Locate every blood parasite and identify its species.
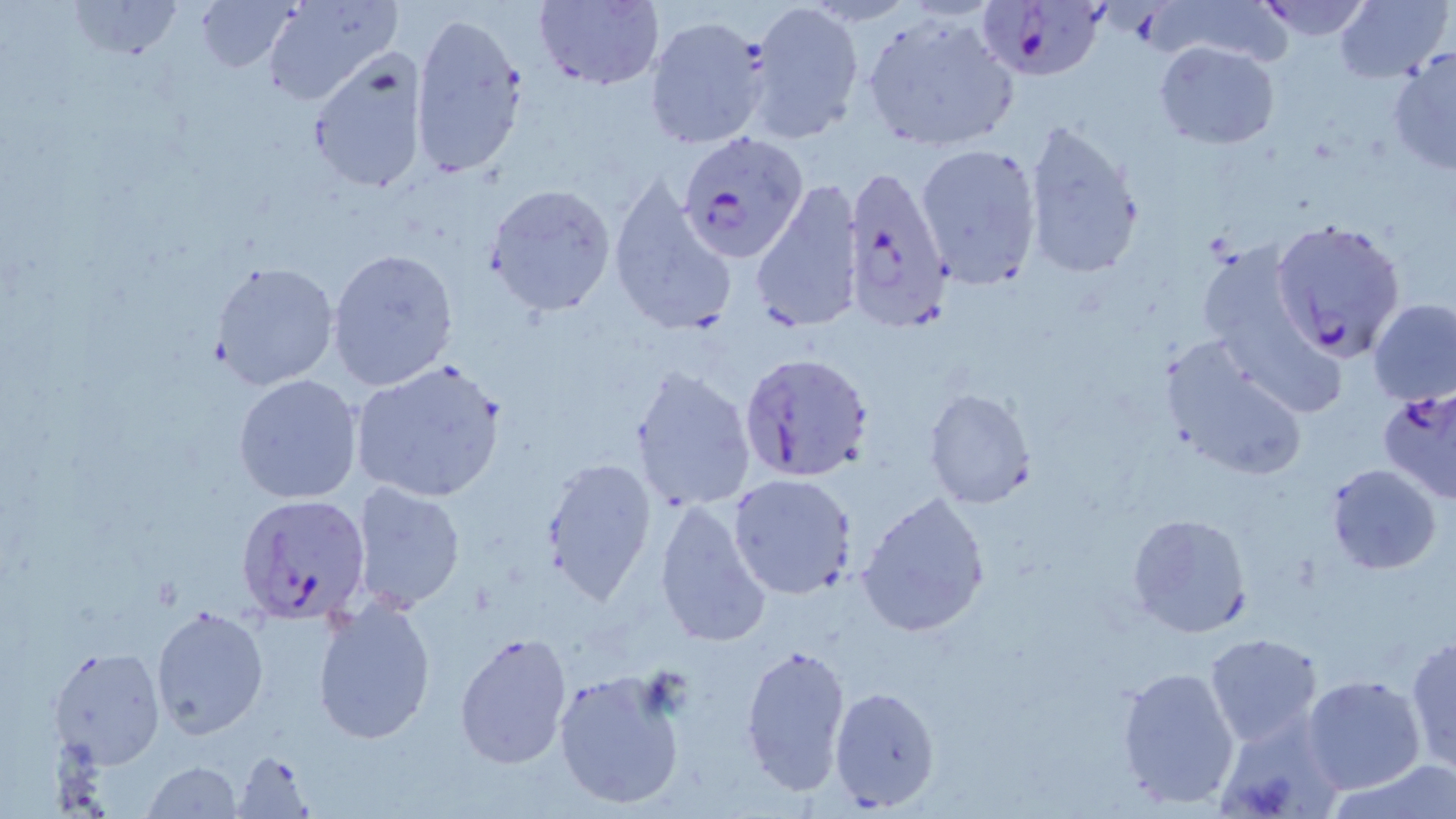

Approximate bounding boxes as (x1,y1)-(x2,y2) corner pairs in pixels.
Plasmodium falciparum-infected red blood cells: (980,1)-(1110,83), (680,132)-(808,262), (839,162)-(956,334), (1270,218)-(1408,361), (739,351)-(877,484), (1374,384)-(1456,509), (236,493)-(372,625).
No Plasmodium ovale, Plasmodium malariae, Plasmodium vivax, Babesia divergens, or Trypanosoma brucei observed.

Summary:
  - Uninfected red blood cell locations: (66,0)-(185,60), (194,0)-(299,74), (260,0)-(400,107), (532,0)-(664,90), (1254,0)-(1377,41), (1336,1)-(1450,82), (745,2)-(866,142), (407,11)-(530,179), (862,13)-(1018,152), (645,15)-(771,150), (1154,40)-(1281,150), (1387,45)-(1456,177), (305,52)-(431,194), (1020,118)-(1145,283), (915,142)-(1042,287), (608,177)-(736,336), (750,180)-(863,334), (486,183)-(617,315), (1194,243)-(1320,371), (325,248)-(458,392), (211,260)-(341,392), (1369,298)-(1456,406), (1160,337)-(1308,480), (349,360)-(508,503), (630,366)-(758,514), (233,374)-(363,503), (922,387)-(1037,509), (541,456)-(658,603), (1325,462)-(1443,574), (728,473)-(857,597), (350,480)-(466,612), (856,490)-(992,636), (654,499)-(774,649), (1126,512)-(1254,639), (311,600)-(437,744), (150,604)-(268,738), (453,631)-(573,769), (1204,632)-(1323,745), (1405,636)-(1456,773), (738,641)-(852,796), (46,645)-(165,769), (1116,666)-(1241,809), (552,669)-(687,810), (1303,674)-(1428,794), (829,685)-(940,811), (1214,711)-(1345,818), (231,751)-(312,817), (1331,760)-(1455,818), (142,761)-(245,817)
  - Slide-level diagnosis: Plasmodium falciparum
  - Field of view: one of a larger specimen
  - Image size: 1456×819 pixels
  - Stain: May-Grünwald-Giemsa
  - Modality: optical microscopy
  - Preparation: thin blood film
  - Magnification: 1000x